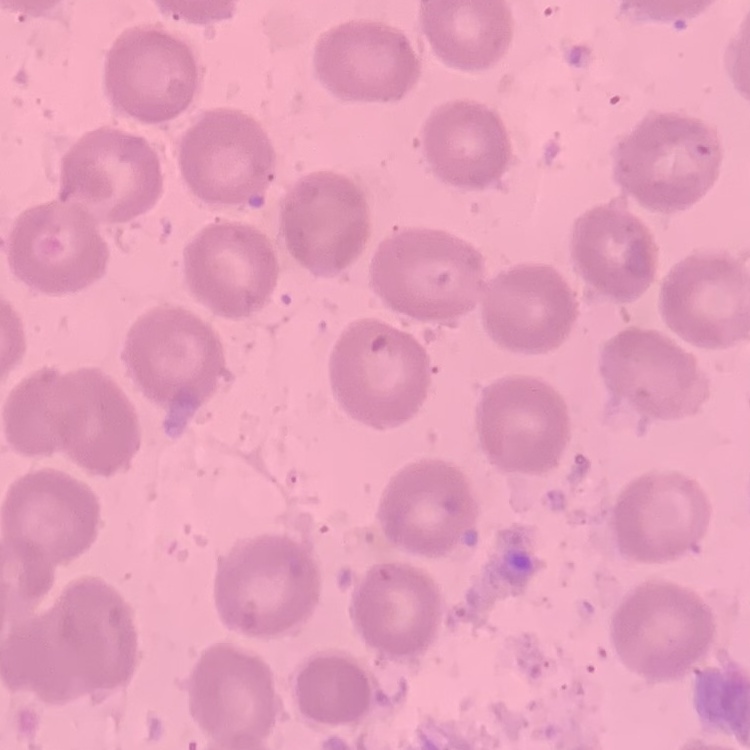

Summary:
  - Red blood cell morphology: no rouleaux formation
  - Stain: Field's or Giemsa
  - Image type: one tile cut from a larger photomicrograph
  - Preparation: thin blood film